Give the position of every malaria parasite.
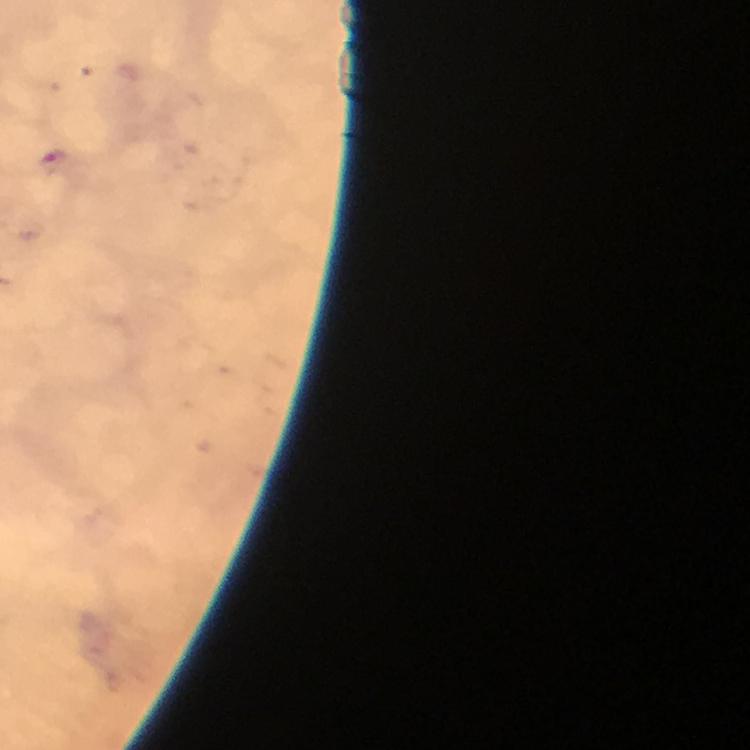

Approximate centers as [x, y] in pixels.
Malaria parasites: [56, 161].

{
  "stain": "Giemsa",
  "image_size": "750×750 pixels",
  "immersion_oil": "applied",
  "capture": "smartphone photograph through a microscope",
  "context": "from a diagnostic examination for malaria",
  "preparation": "thick smear",
  "cropped_from": "a single field of view",
  "magnification": "100x"
}